Point out each Plasmodium parasite.
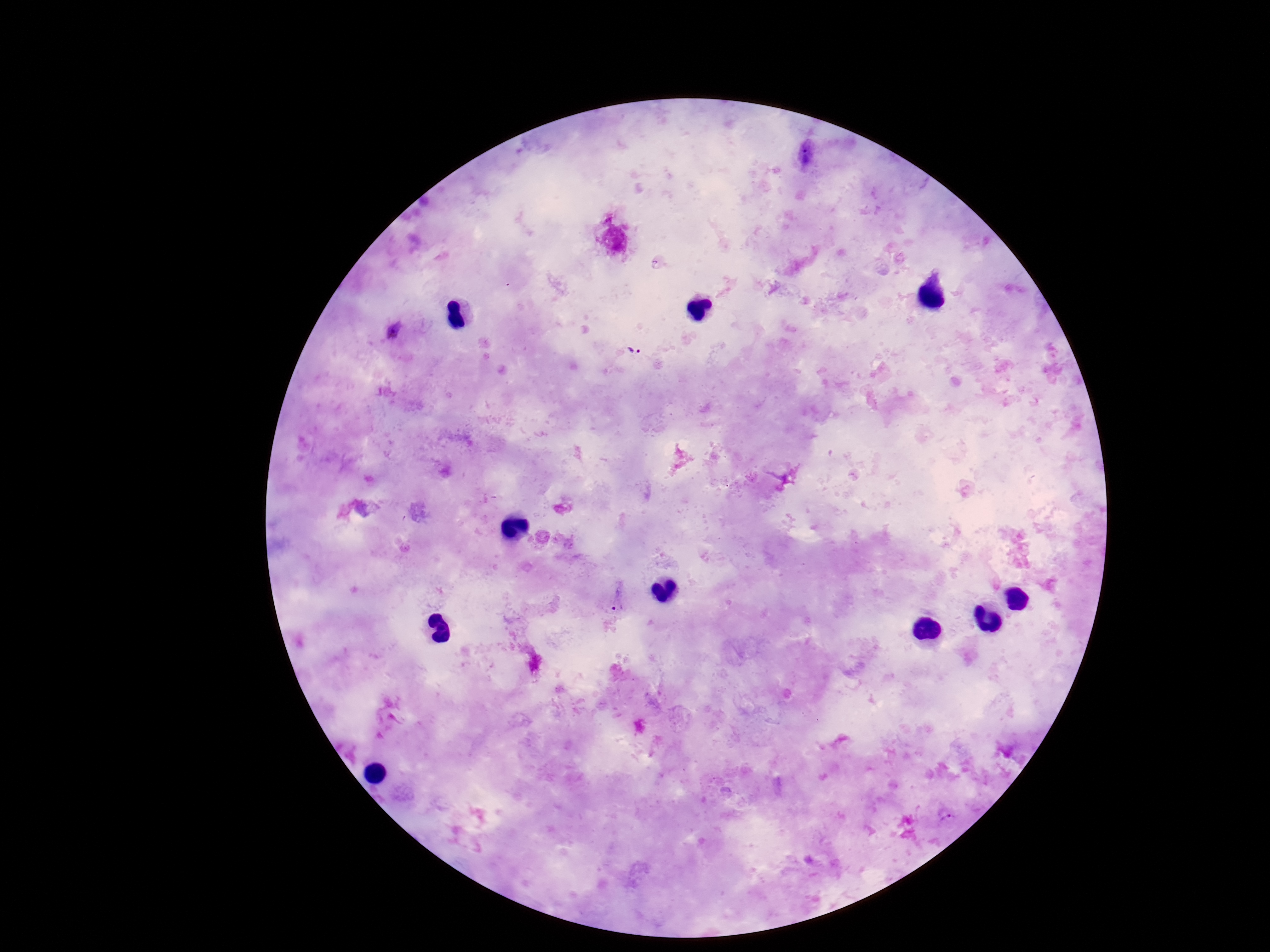

Approximate centers as (x, y) in pixels.
Plasmodium parasites: (806, 153), (394, 330), (632, 349), (617, 598), (946, 816).

Summary:
  - Patient malaria status: positive
  - Field of view: single
  - Image size: 1270×952 pixels
  - Preparation: thick blood smear
  - Magnification: 100x
  - Stain: Giemsa
  - Capture: smartphone camera through the microscope eyepiece